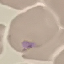
Malaria status: uninfected. Photographed with a smartphone camera at the microscope eyepiece. Giemsa stain. Thin blood film. Automatically extracted cell patch, resized to 64 × 64 pixels.